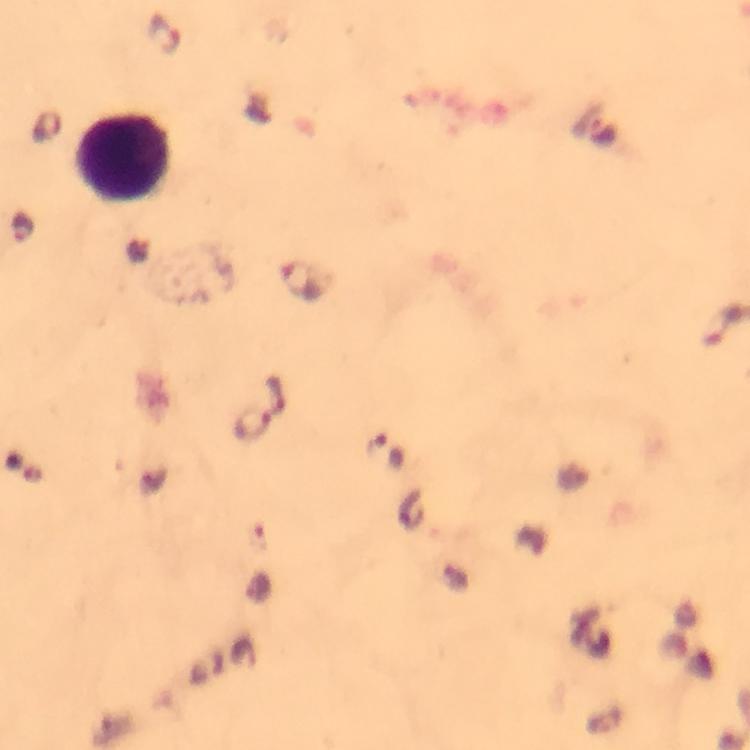
Approximate centers as (x, y) in pixels.
Summary:
  - Leukocyte locations: (123, 158)
  - Plasmodium parasite locations: (164, 34), (601, 133), (24, 228), (300, 280), (277, 397), (250, 424), (386, 453)
  - Stain: Giemsa
  - Preparation: thick smear
  - Magnification: 100x
  - Context: from a diagnostic examination for malaria
  - Capture: smartphone camera through the microscope
  - Image size: 750×750 pixels
  - Immersion oil: used
  - Cropped from: a single field of view